Assess for malaria.
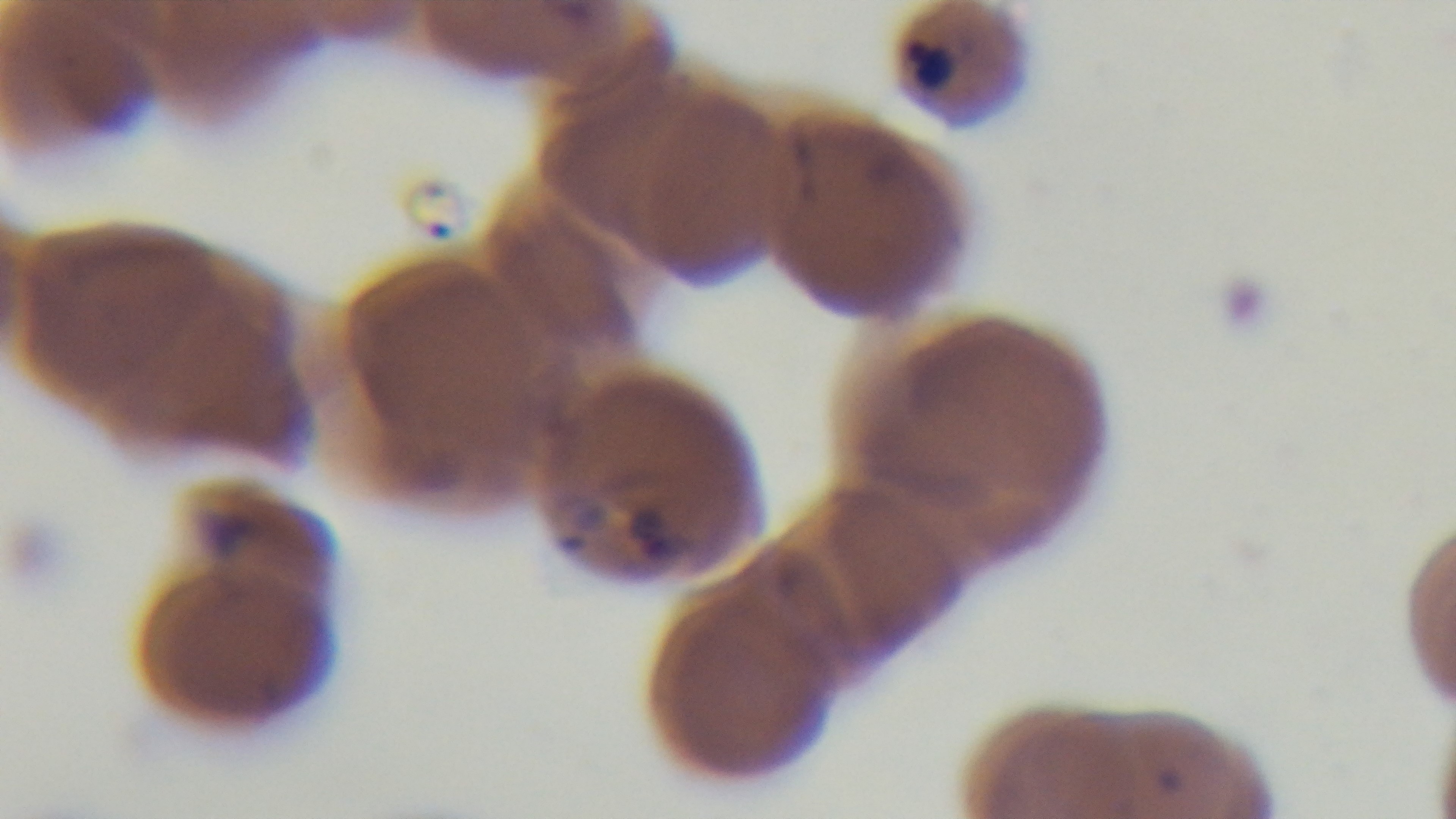

Positive.

Light microscopy. Oil-immersion objective, 100x. Captured with a mounted 4K digital camera. One field from the slide. Giemsa-stained. Preparation: thin blood film.